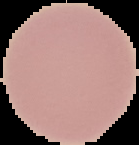

Summary:
  - Preparation: thin blood smear
  - Image type: segmented cell region on a black background
  - Image size: 139×145 pixels
  - Malaria status: uninfected